State which parasite is depicted.
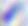

This is Toxoplasma gondii.

modality: micrograph
magnification: 400x